State the blood parasite species.
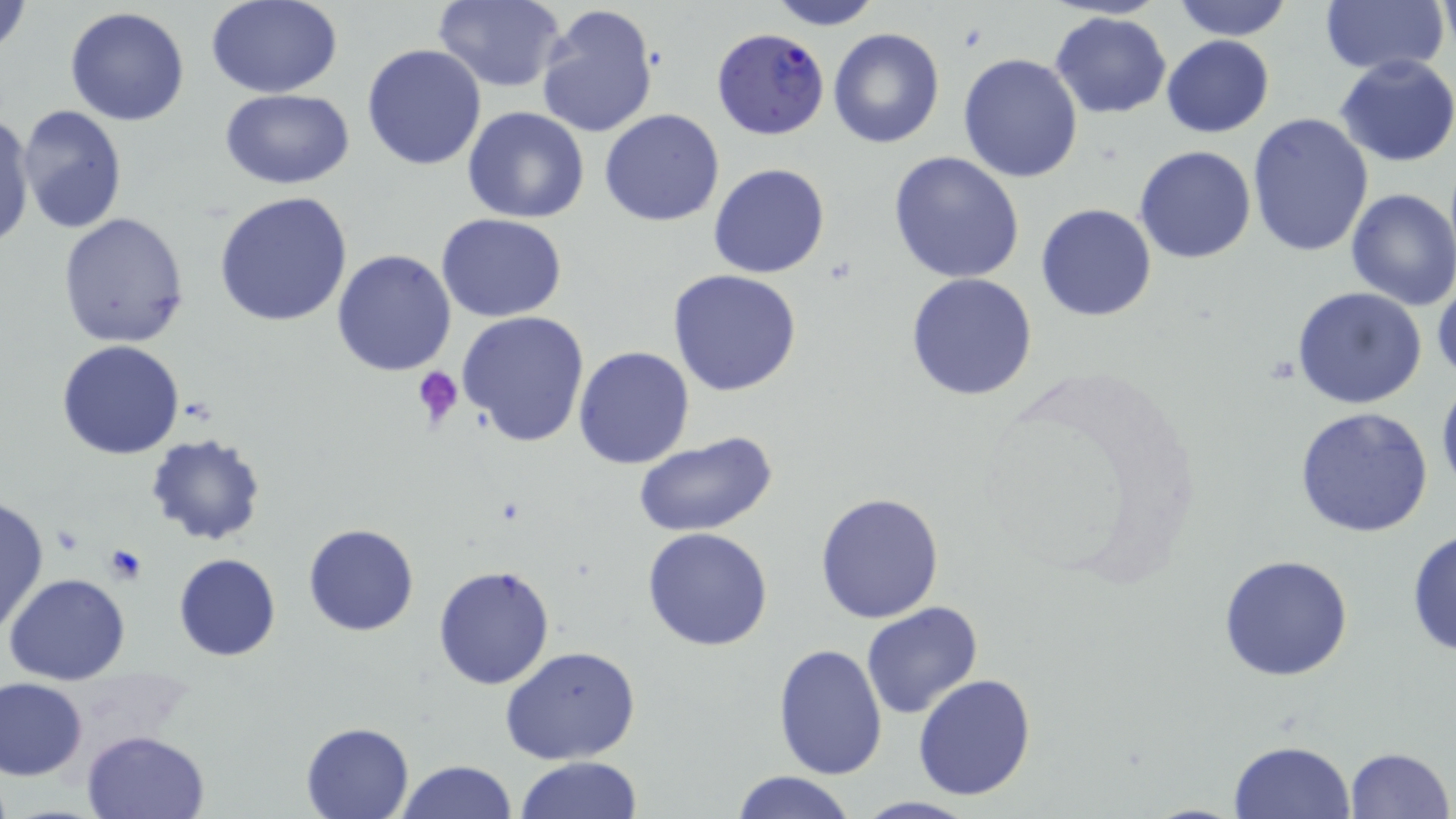
Plasmodium falciparum.

Approximate bounding boxes as (x1,y1)-(x2,y2) corner pairs in pixels. Plasmodium falciparum-infected red blood cell locations: (712,28)-(832,141). Uninfected red blood cell locations: (207,0)-(343,97), (433,0)-(567,92), (1171,0)-(1294,40), (1,1)-(32,62), (766,1)-(882,29), (1319,1)-(1450,75), (535,2)-(659,141), (65,6)-(190,127), (1051,12)-(1172,120), (827,27)-(945,148), (1162,35)-(1275,138), (362,42)-(488,171), (957,52)-(1083,184), (1335,54)-(1456,168), (221,90)-(355,188), (15,104)-(128,233), (463,106)-(590,224), (599,109)-(726,227), (1,111)-(36,248), (1246,112)-(1375,257), (1135,145)-(1256,264), (888,149)-(1025,284), (708,163)-(831,279), (1345,188)-(1456,310), (212,190)-(355,327), (1036,204)-(1157,321), (59,212)-(190,348), (437,214)-(567,323), (332,249)-(457,375), (669,269)-(802,396), (905,272)-(1038,401), (1291,287)-(1427,409), (456,310)-(590,448), (57,339)-(185,459), (573,345)-(695,469), (1435,375)-(1456,500), (1295,406)-(1436,539), (632,432)-(776,537), (145,433)-(267,548), (814,492)-(945,624), (0,495)-(48,636), (303,523)-(419,636), (641,527)-(773,651), (1406,527)-(1456,661), (173,554)-(281,661), (1218,554)-(1354,682), (433,564)-(556,690), (5,573)-(130,685), (860,600)-(984,720), (773,644)-(889,778), (500,646)-(643,766), (913,673)-(1037,801), (0,677)-(89,780), (300,721)-(416,818), (83,729)-(211,819), (1228,740)-(1355,819), (1342,747)-(1452,819), (515,755)-(644,818), (395,759)-(516,818), (729,770)-(857,819), (851,795)-(978,817). Platelet locations: (412,366)-(465,430), (99,544)-(149,586). Thin blood film. 1000x magnification. One field of a larger specimen. May-Grünwald-Giemsa stain. Optical microscopy. Image is 1456×819 pixels.